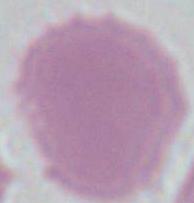 1000x magnification. Photomicrograph. A red blood cell is seen.